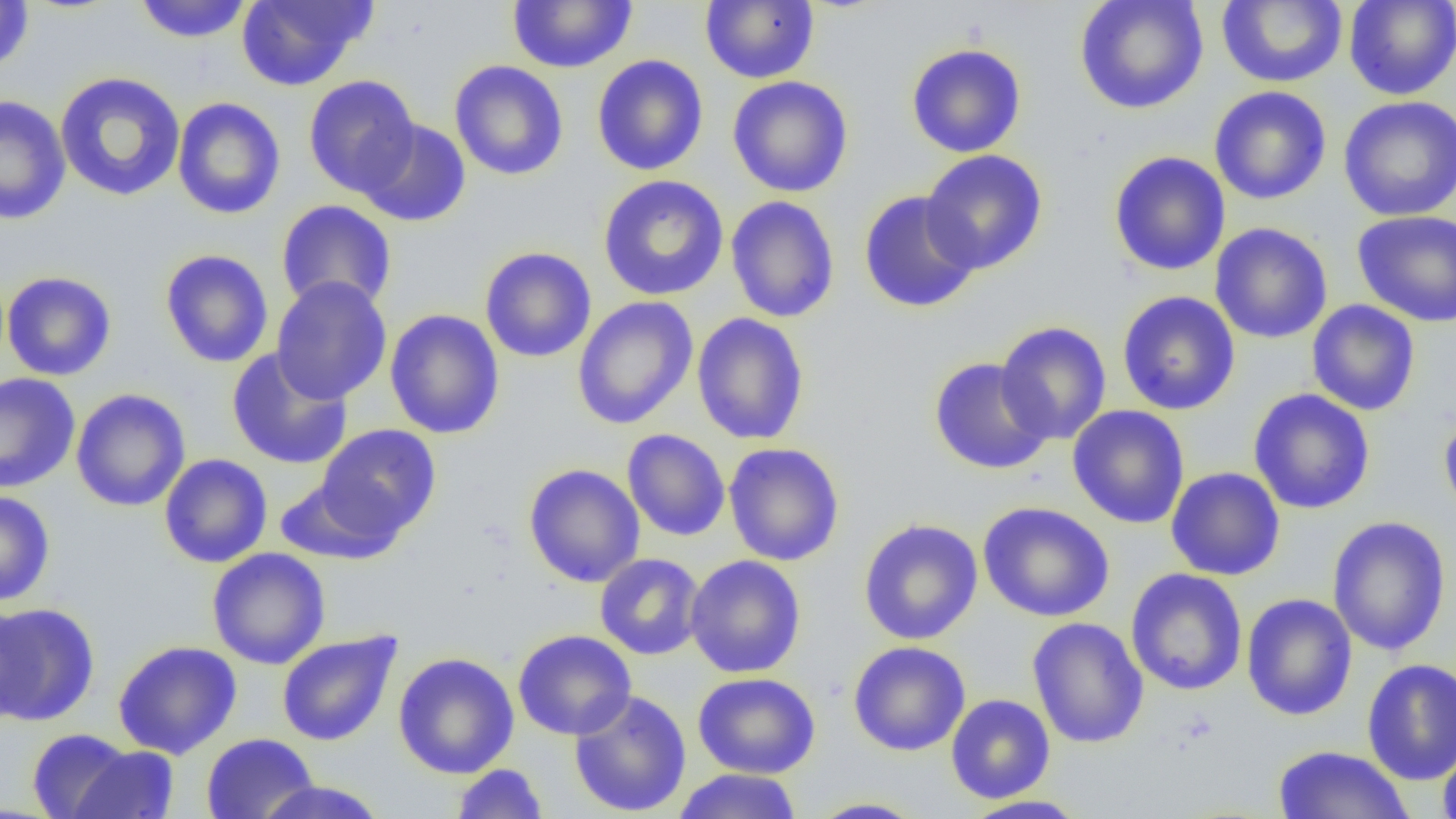

Approximate bounding boxes as (x1, y1, x2, y2) in pixels. Uninfected red blood cell locations: (236, 0, 376, 91), (506, 0, 637, 73), (1074, 0, 1209, 114), (1216, 0, 1348, 88), (1344, 0, 1456, 100), (0, 1, 34, 74), (132, 1, 256, 44), (701, 1, 819, 84), (905, 43, 1027, 158), (592, 54, 709, 176), (449, 60, 569, 181), (54, 71, 186, 202), (303, 75, 420, 197), (727, 76, 854, 197), (1209, 86, 1332, 205), (0, 94, 72, 224), (1337, 95, 1456, 221), (171, 97, 286, 220), (356, 118, 472, 227), (920, 149, 1048, 275), (1108, 151, 1230, 276), (597, 175, 729, 301), (858, 190, 981, 313), (725, 195, 840, 323), (276, 200, 397, 313), (1351, 210, 1456, 326), (1210, 222, 1333, 344), (479, 246, 597, 363), (159, 249, 274, 368), (1, 271, 117, 381), (271, 277, 391, 405), (1117, 291, 1241, 416), (572, 296, 698, 430), (1306, 300, 1421, 416), (385, 309, 505, 439), (691, 313, 809, 445), (995, 321, 1112, 446), (227, 347, 353, 470), (928, 357, 1053, 475), (0, 372, 80, 493), (1248, 388, 1376, 514), (71, 389, 191, 511), (1067, 404, 1190, 529), (1439, 409, 1456, 529), (316, 423, 441, 540), (622, 428, 731, 541), (723, 442, 845, 566), (159, 453, 272, 568), (522, 463, 645, 587), (1166, 467, 1285, 581), (273, 476, 401, 564), (0, 490, 55, 606), (977, 501, 1115, 622), (1327, 516, 1451, 656), (857, 518, 984, 645), (206, 547, 331, 670), (595, 553, 705, 660), (684, 555, 806, 678), (1125, 568, 1248, 696), (1241, 593, 1357, 721), (0, 597, 30, 726), (0, 601, 101, 726), (1027, 617, 1149, 749), (513, 629, 636, 740), (276, 630, 402, 747), (113, 640, 242, 759), (848, 641, 971, 756), (393, 652, 520, 778), (1361, 658, 1456, 785), (692, 672, 821, 779), (569, 690, 692, 817), (945, 693, 1055, 804), (26, 728, 138, 818), (201, 733, 319, 819), (1437, 742, 1456, 819), (65, 743, 180, 819), (1272, 744, 1414, 819), (451, 763, 550, 819), (670, 768, 803, 819), (252, 780, 390, 819), (960, 794, 1091, 818), (804, 797, 928, 818). Slide-level diagnosis: negative for blood parasites. One field of a larger specimen. Thin blood smear. Image is 1456×819 pixels. Light microscopy. Captured at 1000x magnification.